Name the parasite shown.
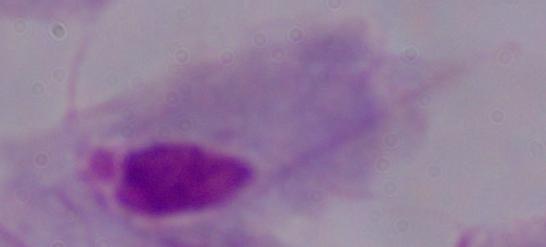
A trichomonad.

Summary:
  - Modality: micrograph
  - Magnification: 1000x